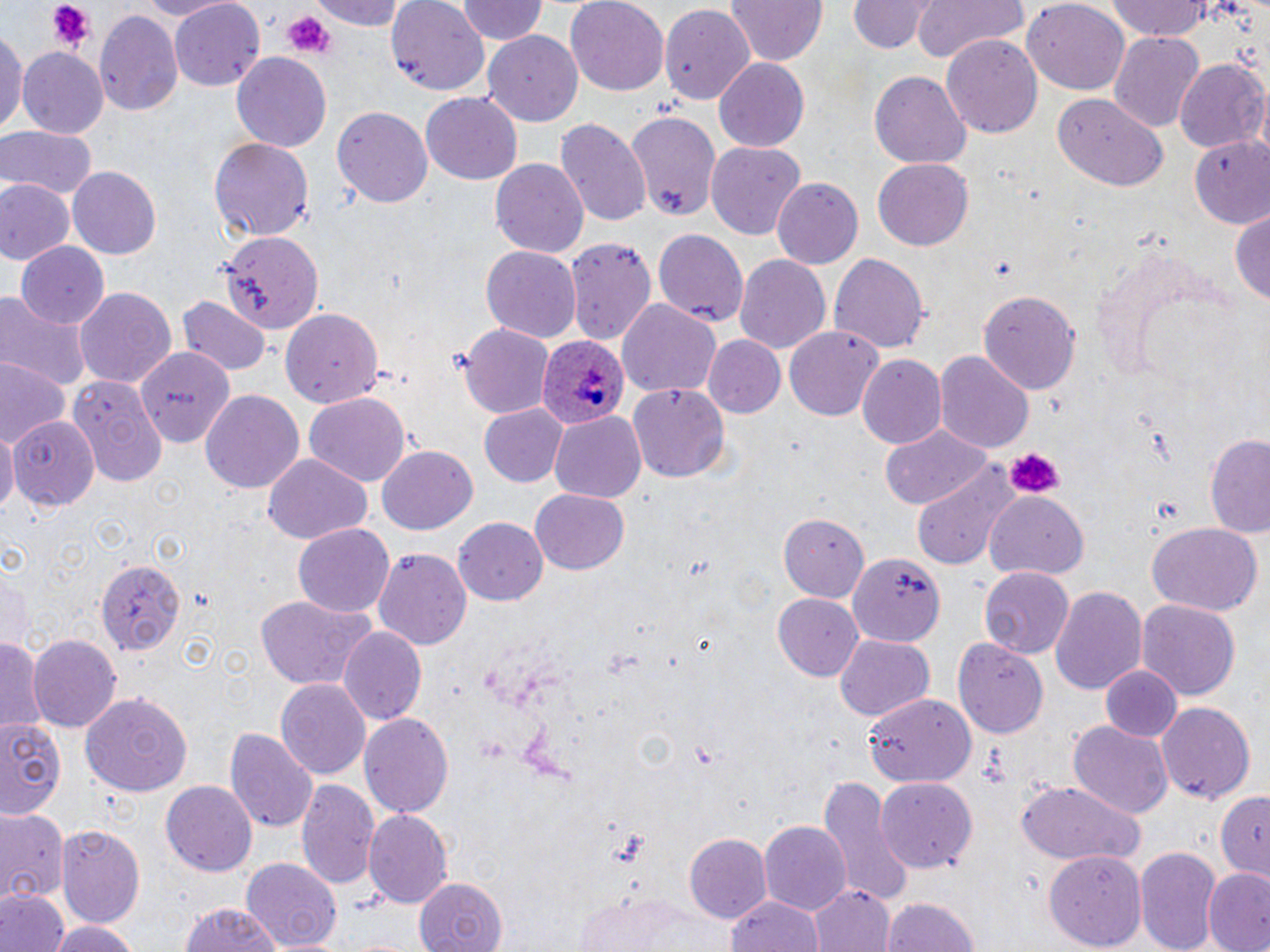

Approximate bounding boxes as named x1/y1/x2/y2 corners in pixels. Uninfected red blood cell locations: (x1=134, y1=0, x2=232, y2=19), (x1=314, y1=0, x2=409, y2=30), (x1=455, y1=0, x2=546, y2=45), (x1=565, y1=0, x2=668, y2=93), (x1=727, y1=0, x2=827, y2=66), (x1=848, y1=0, x2=933, y2=52), (x1=911, y1=0, x2=1029, y2=66), (x1=1106, y1=0, x2=1218, y2=42), (x1=387, y1=2, x2=488, y2=94), (x1=1022, y1=2, x2=1131, y2=93), (x1=169, y1=3, x2=265, y2=91), (x1=660, y1=4, x2=755, y2=107), (x1=94, y1=9, x2=183, y2=118), (x1=0, y1=23, x2=24, y2=137), (x1=481, y1=31, x2=583, y2=125), (x1=1108, y1=31, x2=1204, y2=134), (x1=941, y1=34, x2=1043, y2=139), (x1=17, y1=46, x2=108, y2=136), (x1=231, y1=53, x2=332, y2=153), (x1=713, y1=58, x2=813, y2=153), (x1=1176, y1=60, x2=1268, y2=154), (x1=869, y1=73, x2=972, y2=169), (x1=420, y1=93, x2=523, y2=184), (x1=1053, y1=95, x2=1166, y2=191), (x1=332, y1=106, x2=433, y2=208), (x1=624, y1=111, x2=721, y2=223), (x1=556, y1=117, x2=651, y2=228), (x1=0, y1=129, x2=96, y2=202), (x1=1190, y1=134, x2=1270, y2=226), (x1=209, y1=136, x2=313, y2=239), (x1=706, y1=141, x2=803, y2=239), (x1=489, y1=157, x2=589, y2=259), (x1=872, y1=158, x2=974, y2=249), (x1=68, y1=166, x2=161, y2=258), (x1=771, y1=178, x2=863, y2=269), (x1=1, y1=181, x2=71, y2=268), (x1=1231, y1=212, x2=1270, y2=307), (x1=653, y1=229, x2=748, y2=330), (x1=220, y1=231, x2=325, y2=332), (x1=566, y1=236, x2=657, y2=348), (x1=13, y1=241, x2=110, y2=329), (x1=1086, y1=244, x2=1241, y2=388), (x1=481, y1=246, x2=581, y2=341), (x1=828, y1=251, x2=931, y2=355), (x1=734, y1=254, x2=831, y2=355), (x1=73, y1=285, x2=177, y2=389), (x1=0, y1=288, x2=88, y2=392), (x1=977, y1=288, x2=1081, y2=393), (x1=178, y1=296, x2=270, y2=377), (x1=615, y1=298, x2=722, y2=401), (x1=278, y1=307, x2=381, y2=406), (x1=459, y1=323, x2=555, y2=420), (x1=783, y1=324, x2=883, y2=421), (x1=703, y1=336, x2=785, y2=418), (x1=136, y1=343, x2=232, y2=445), (x1=933, y1=349, x2=1034, y2=453), (x1=857, y1=354, x2=947, y2=449), (x1=0, y1=357, x2=70, y2=450), (x1=70, y1=377, x2=167, y2=487), (x1=628, y1=381, x2=730, y2=480), (x1=198, y1=389, x2=306, y2=496), (x1=303, y1=392, x2=412, y2=485), (x1=480, y1=404, x2=568, y2=486), (x1=548, y1=413, x2=646, y2=504), (x1=9, y1=417, x2=99, y2=508), (x1=880, y1=426, x2=989, y2=511), (x1=1, y1=427, x2=17, y2=521), (x1=1205, y1=433, x2=1270, y2=539), (x1=378, y1=447, x2=477, y2=534), (x1=262, y1=453, x2=372, y2=545), (x1=912, y1=463, x2=1022, y2=570), (x1=530, y1=488, x2=630, y2=573), (x1=986, y1=492, x2=1089, y2=579), (x1=778, y1=510, x2=872, y2=601), (x1=454, y1=517, x2=548, y2=606), (x1=1146, y1=520, x2=1264, y2=616), (x1=292, y1=523, x2=395, y2=619), (x1=374, y1=549, x2=470, y2=651), (x1=849, y1=553, x2=944, y2=647), (x1=97, y1=558, x2=184, y2=653), (x1=1, y1=564, x2=32, y2=654), (x1=978, y1=568, x2=1075, y2=657), (x1=1050, y1=583, x2=1146, y2=694), (x1=255, y1=593, x2=379, y2=691), (x1=772, y1=593, x2=863, y2=680), (x1=1136, y1=597, x2=1243, y2=698), (x1=341, y1=625, x2=428, y2=725), (x1=0, y1=633, x2=44, y2=732), (x1=26, y1=633, x2=120, y2=731), (x1=833, y1=635, x2=935, y2=721), (x1=955, y1=639, x2=1049, y2=737), (x1=1099, y1=666, x2=1181, y2=743), (x1=277, y1=678, x2=371, y2=781), (x1=81, y1=691, x2=192, y2=796), (x1=865, y1=697, x2=975, y2=790), (x1=1155, y1=700, x2=1256, y2=805), (x1=358, y1=711, x2=454, y2=818), (x1=0, y1=714, x2=71, y2=820), (x1=1069, y1=721, x2=1172, y2=819), (x1=225, y1=727, x2=318, y2=833), (x1=818, y1=775, x2=911, y2=907), (x1=875, y1=777, x2=977, y2=875), (x1=1014, y1=777, x2=1146, y2=871), (x1=297, y1=778, x2=381, y2=895), (x1=161, y1=782, x2=257, y2=875), (x1=1214, y1=790, x2=1270, y2=879), (x1=362, y1=808, x2=452, y2=908), (x1=0, y1=810, x2=70, y2=898), (x1=758, y1=821, x2=850, y2=916), (x1=57, y1=824, x2=146, y2=925), (x1=685, y1=833, x2=770, y2=924), (x1=1136, y1=845, x2=1223, y2=952), (x1=1046, y1=850, x2=1146, y2=950), (x1=242, y1=858, x2=342, y2=951), (x1=1203, y1=870, x2=1270, y2=952), (x1=410, y1=876, x2=509, y2=952), (x1=808, y1=884, x2=895, y2=952), (x1=2, y1=889, x2=69, y2=952), (x1=724, y1=893, x2=825, y2=952), (x1=571, y1=894, x2=726, y2=952), (x1=882, y1=895, x2=981, y2=952), (x1=177, y1=901, x2=289, y2=952), (x1=47, y1=920, x2=144, y2=952). Plasmodium ovale-infected red blood cell locations: (x1=538, y1=333, x2=628, y2=431). Platelet locations: (x1=49, y1=2, x2=91, y2=51), (x1=284, y1=11, x2=334, y2=57), (x1=1004, y1=448, x2=1065, y2=500). Slide-level diagnosis: Plasmodium ovale. Image is 1270×952 pixels. May-Grünwald-Giemsa stain. Single field of view. Thin blood film. Optical microscopy. 1000x magnification.